Identify the parasite.
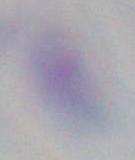

This is Toxoplasma gondii.

Micrograph. Captured at 1000x magnification.